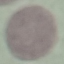
result: negative for malaria parasites
capture: smartphone camera at the microscope eyepiece
stain: Giemsa
image_type: cell patch, automatically extracted from a larger field of view and resized to 64 × 64 pixels
preparation: thin blood smear